Identify the cell.
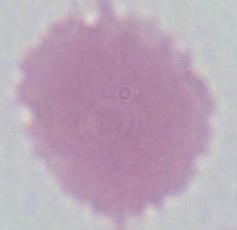
An erythrocyte.

magnification = 1000x
modality = micrograph